Locate every blood parasite and identify its species.
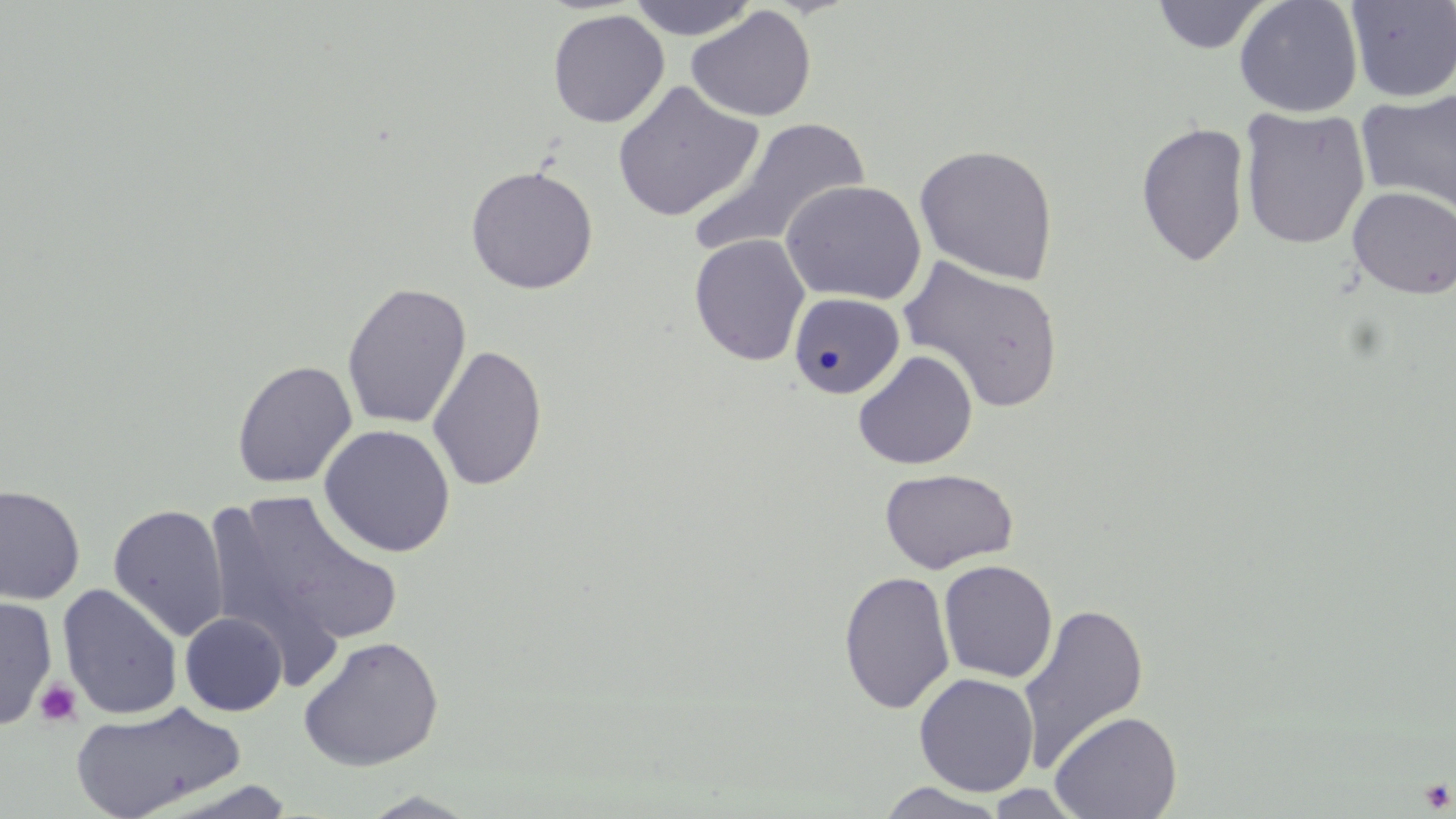
No blood parasites seen.

Summary:
  - Coordinate format: approximate bounding boxes as (x1,y1)-(x2,y2) corner pairs in pixels
  - Platelet locations: (35,678)-(83,727), (1420,780)-(1454,813)
  - Uninfected red blood cell locations: (626,0)-(759,41), (1151,0)-(1273,54), (1234,0)-(1364,117), (1345,0)-(1456,102), (686,6)-(816,122), (547,9)-(670,129), (612,80)-(763,223), (1357,89)-(1456,215), (1238,106)-(1371,250), (688,117)-(873,259), (1135,121)-(1250,268), (914,144)-(1059,285), (465,165)-(598,294), (781,179)-(926,305), (1347,186)-(1456,299), (689,233)-(810,366), (896,254)-(1065,415), (342,282)-(472,430), (788,291)-(907,400), (427,344)-(548,491), (853,350)-(978,470), (231,360)-(357,489), (318,424)-(456,557), (879,468)-(1019,574), (0,485)-(86,605), (213,489)-(404,662), (108,503)-(229,641), (937,559)-(1058,683), (838,570)-(956,714), (57,584)-(183,720), (0,596)-(58,729), (1017,600)-(1149,774), (180,612)-(287,716), (297,635)-(444,772), (914,672)-(1039,796), (70,701)-(245,818), (1049,710)-(1183,819), (874,782)-(1011,818), (984,784)-(1088,818), (356,791)-(483,818)
  - Slide-level diagnosis: no evidence of blood parasites
  - Modality: light microscopy
  - Preparation: thin blood smear
  - Field of view: single
  - Image size: 1456×819 pixels
  - Magnification: 1000x
  - Stain: May-Grünwald-Giemsa